Assess this cell for malaria.
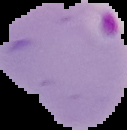

Parasitized.

The area outside the segmented cell region is set to black. From a thin blood smear. Image is 127×130 pixels.